Classify this cell by malaria status.
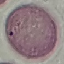

Uninfected.

Giemsa-stained preparation. Thin blood smear. Acquired by smartphone through the microscope eyepiece. Cell patch, automatically extracted from a larger field of view and resized to 64 × 64 pixels.